Identify the blood parasite species.
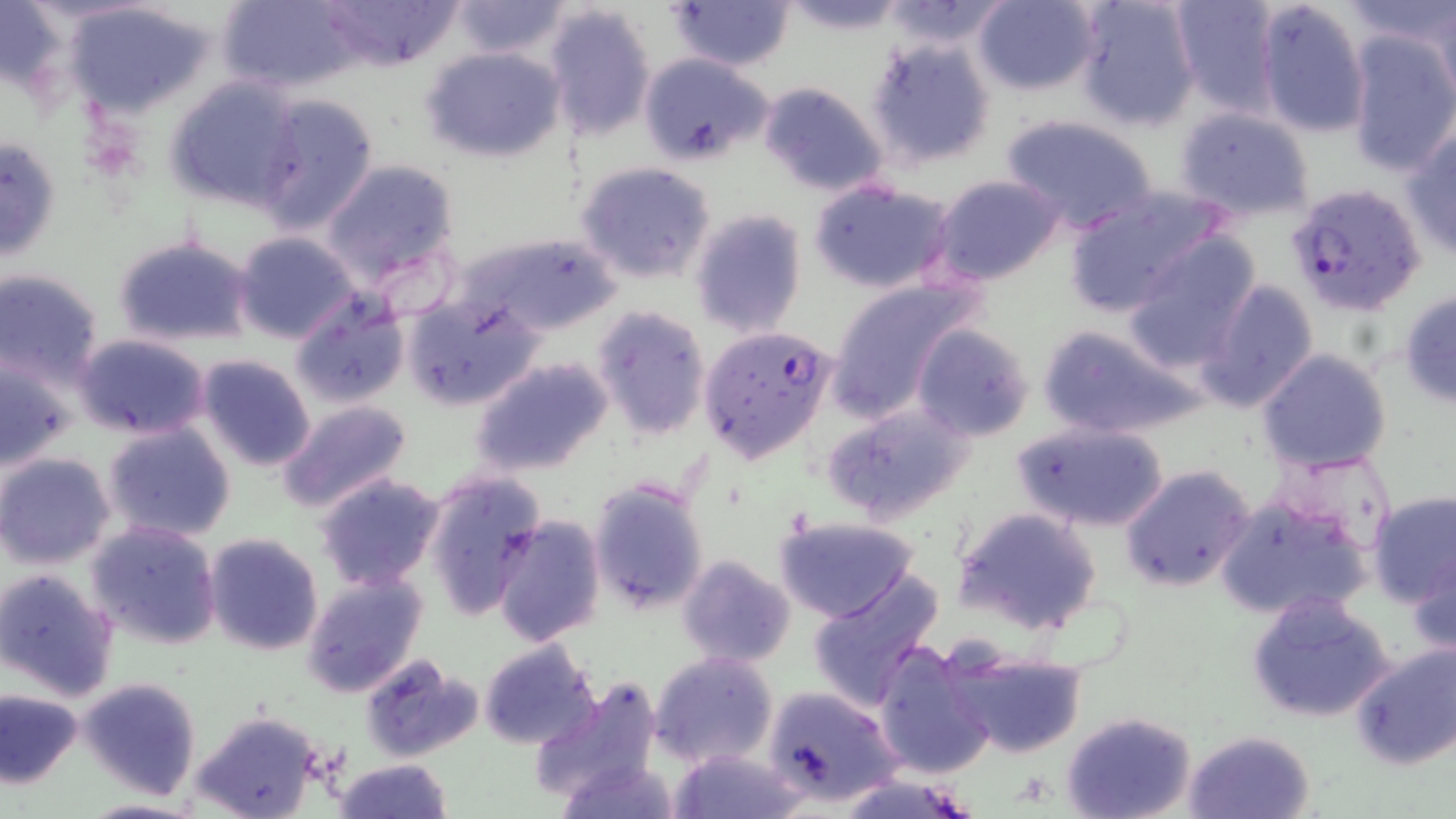
Plasmodium falciparum.

stain = May-Grünwald-Giemsa
modality = optical microscopy
Plasmodium falciparum-infected red blood cell locations = approximate bounding boxes as named x1/y1/x2/y2 corners in pixels: (x1=1288, y1=182, x2=1426, y2=315), (x1=696, y1=325, x2=839, y2=464)
image size = 1456×819 pixels
field of view = single
magnification = 1000x
uninfected red blood cell locations = approximate bounding boxes as named x1/y1/x2/y2 corners in pixels: (x1=215, y1=0, x2=363, y2=94), (x1=314, y1=0, x2=465, y2=70), (x1=664, y1=0, x2=797, y2=71), (x1=781, y1=0, x2=911, y2=34), (x1=971, y1=0, x2=1101, y2=95), (x1=1072, y1=0, x2=1203, y2=129), (x1=1169, y1=0, x2=1279, y2=114), (x1=1253, y1=0, x2=1372, y2=139), (x1=1423, y1=0, x2=1455, y2=109), (x1=448, y1=1, x2=572, y2=60), (x1=880, y1=1, x2=1014, y2=50), (x1=1344, y1=1, x2=1456, y2=60), (x1=61, y1=2, x2=218, y2=117), (x1=544, y1=4, x2=658, y2=142), (x1=1345, y1=32, x2=1456, y2=177), (x1=866, y1=40, x2=995, y2=171), (x1=422, y1=46, x2=566, y2=162), (x1=639, y1=53, x2=775, y2=166), (x1=164, y1=75, x2=306, y2=211), (x1=758, y1=82, x2=888, y2=199), (x1=252, y1=95, x2=379, y2=235), (x1=1173, y1=106, x2=1317, y2=224), (x1=1000, y1=114, x2=1158, y2=235), (x1=1402, y1=128, x2=1456, y2=260), (x1=0, y1=133, x2=63, y2=267), (x1=321, y1=159, x2=462, y2=291), (x1=576, y1=162, x2=716, y2=284), (x1=931, y1=174, x2=1065, y2=286), (x1=809, y1=180, x2=956, y2=295), (x1=1062, y1=186, x2=1228, y2=318), (x1=690, y1=208, x2=806, y2=338), (x1=458, y1=230, x2=619, y2=338), (x1=233, y1=231, x2=360, y2=343), (x1=112, y1=235, x2=257, y2=348), (x1=1124, y1=235, x2=1261, y2=369), (x1=2, y1=269, x2=107, y2=386), (x1=823, y1=279, x2=972, y2=417), (x1=1199, y1=279, x2=1320, y2=413), (x1=1398, y1=290, x2=1456, y2=409), (x1=402, y1=292, x2=542, y2=411), (x1=289, y1=296, x2=409, y2=410), (x1=588, y1=306, x2=711, y2=441), (x1=1034, y1=321, x2=1197, y2=441), (x1=911, y1=324, x2=1033, y2=441), (x1=73, y1=333, x2=213, y2=440), (x1=1256, y1=348, x2=1393, y2=475), (x1=0, y1=353, x2=81, y2=472), (x1=194, y1=355, x2=318, y2=473), (x1=469, y1=356, x2=616, y2=479), (x1=276, y1=400, x2=413, y2=516), (x1=820, y1=402, x2=974, y2=525), (x1=1009, y1=418, x2=1169, y2=532), (x1=102, y1=421, x2=236, y2=544), (x1=1274, y1=450, x2=1399, y2=554), (x1=1, y1=453, x2=117, y2=570), (x1=1121, y1=464, x2=1256, y2=593), (x1=423, y1=469, x2=547, y2=622), (x1=314, y1=473, x2=445, y2=591), (x1=587, y1=478, x2=710, y2=616), (x1=1366, y1=489, x2=1455, y2=608), (x1=1214, y1=494, x2=1371, y2=622), (x1=953, y1=505, x2=1103, y2=636), (x1=773, y1=515, x2=920, y2=623), (x1=491, y1=516, x2=606, y2=646), (x1=86, y1=521, x2=224, y2=649), (x1=204, y1=532, x2=326, y2=657), (x1=1409, y1=547, x2=1456, y2=659), (x1=678, y1=555, x2=796, y2=670), (x1=0, y1=567, x2=120, y2=700), (x1=806, y1=570, x2=943, y2=711), (x1=302, y1=572, x2=428, y2=700), (x1=1246, y1=593, x2=1397, y2=725), (x1=479, y1=639, x2=600, y2=751), (x1=875, y1=641, x2=995, y2=779), (x1=1349, y1=642, x2=1456, y2=771), (x1=942, y1=643, x2=1089, y2=761), (x1=650, y1=652, x2=779, y2=769), (x1=362, y1=655, x2=483, y2=762), (x1=655, y1=669, x2=896, y2=789), (x1=76, y1=675, x2=202, y2=801), (x1=527, y1=676, x2=665, y2=807), (x1=762, y1=684, x2=902, y2=807), (x1=1, y1=688, x2=83, y2=788), (x1=190, y1=710, x2=323, y2=819), (x1=1061, y1=712, x2=1197, y2=819), (x1=1183, y1=729, x2=1316, y2=819), (x1=671, y1=747, x2=806, y2=819), (x1=333, y1=757, x2=453, y2=818), (x1=557, y1=761, x2=684, y2=819)
preparation = thin blood film